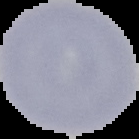
malaria_status: uninfected
image_type: segmented cell region on a black background
image_size: 139×139 pixels
preparation: thin blood film